Report the malaria status of this cell.
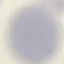
Uninfected.

Giemsa-stained preparation. Photographed with a smartphone camera at the microscope eyepiece. Thin blood smear. Automatically extracted cell patch, resized to 64 × 64 pixels.